Assess this cell for malaria.
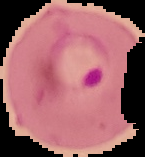

It is parasitized.

image type = segmented cell region on a black background
preparation = thin blood film
image size = 145×157 pixels